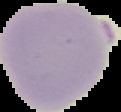 The area outside the segmented cell region is set to black. From a thin blood smear. Image is 121×112 pixels. Result: Plasmodium parasites detected.